Assess the morphology of the red blood cells.
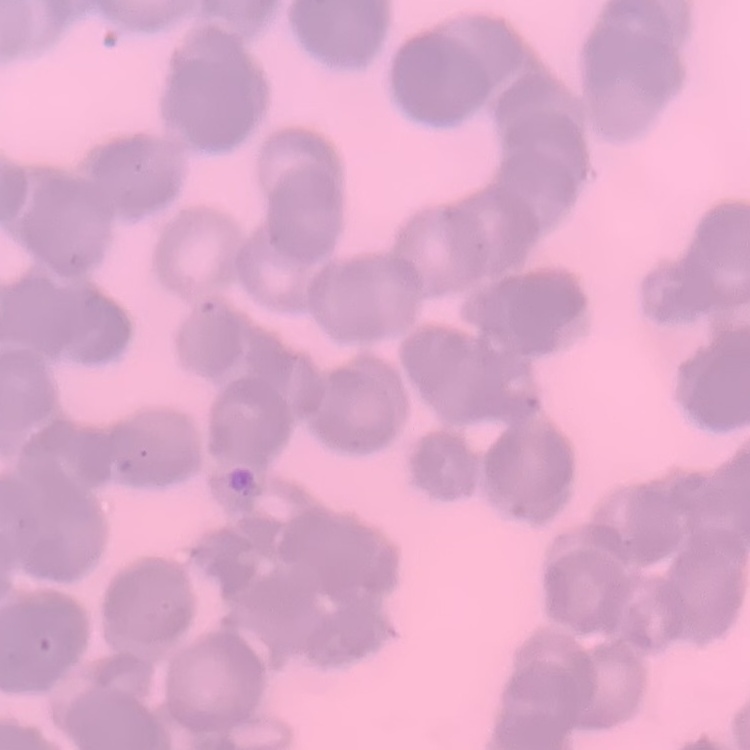
Rouleaux formation.

Stained with either Field's or Giemsa. Square crop of a larger photomicrograph. Thin peripheral smear.